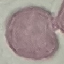
Summary:
  - Malaria status: uninfected
  - Image type: cell patch, automatically extracted from a larger field of view and resized to 64 × 64 pixels
  - Preparation: thin blood film
  - Capture: smartphone camera at the microscope eyepiece
  - Stain: Giemsa